Give the preparation type.
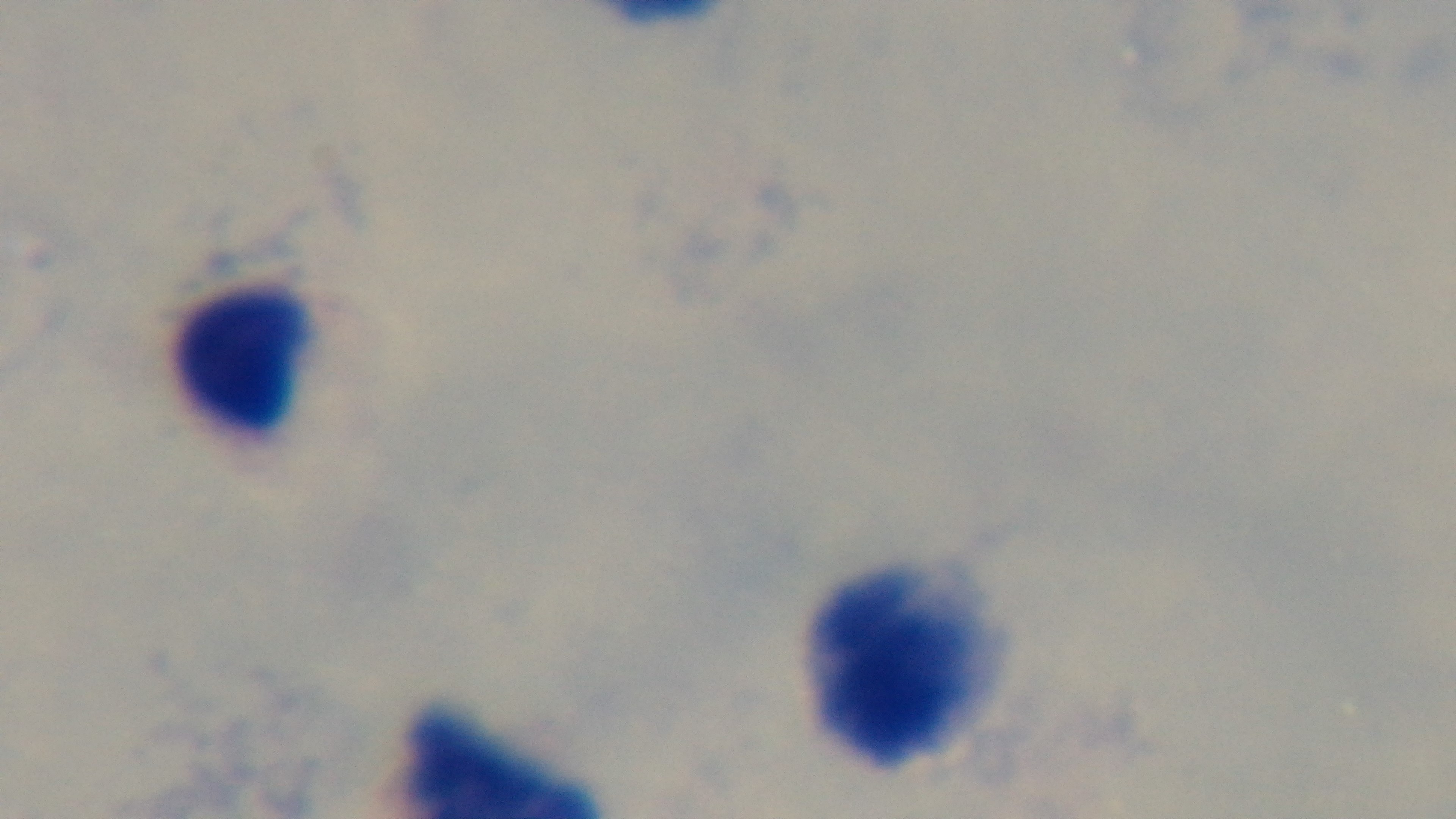
It is a thick blood film.

{
  "objective": "100x oil immersion",
  "stain": "Giemsa",
  "field_of_view": "single",
  "modality": "light microscopy",
  "capture": "mounted 4K digital camera",
  "malaria_status": "negative"
}